Classify this cell by malaria status.
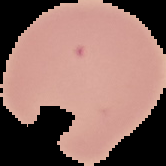

Uninfected.

image size = 166×166 pixels
preparation = thin blood smear
image type = segmented cell region on a black background